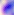

identification = Toxoplasma gondii
magnification = 400x
modality = photomicrograph